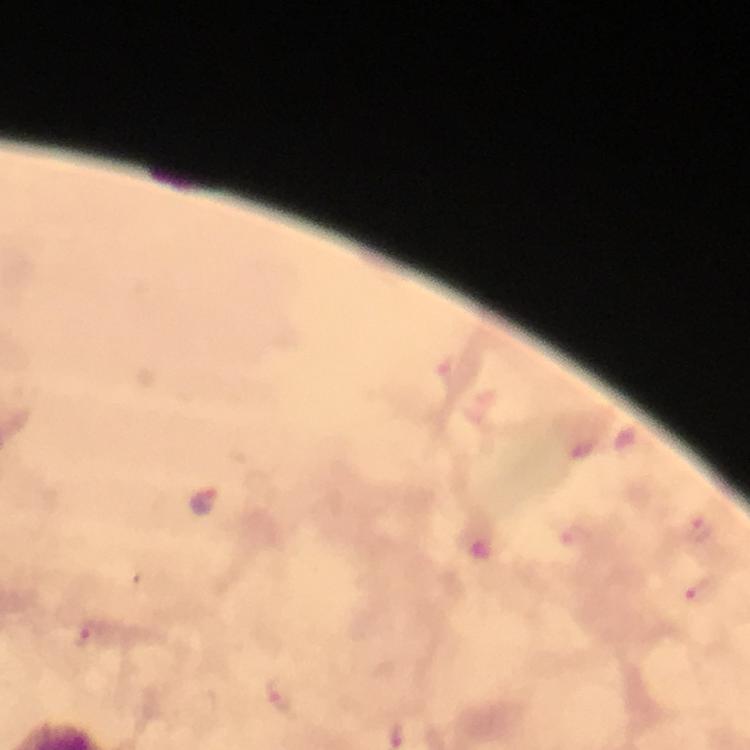

Approximate centers as (x, y) in pixels.
Summary:
  - Malaria parasite locations: (204, 502), (700, 530), (706, 591), (86, 636), (280, 695)
  - Cropped from: one field of view
  - Context: from a diagnostic examination for malaria
  - Image size: 750×750 pixels
  - Stain: Giemsa
  - Magnification: 100x
  - Preparation: thick blood smear
  - Capture: smartphone photograph through a microscope
  - Immersion oil: applied